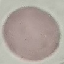

Result: no malaria parasites detected. Automatically extracted cell patch, resized to 64 × 64 pixels. Thin smear of blood. Photographed with a smartphone camera at the microscope eyepiece. Giemsa-stained preparation.